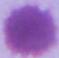
Summary:
  - Magnification: 1000x
  - Modality: photomicrograph
  - Identification: erythrocyte